Identify the parasite.
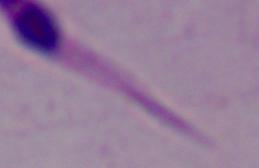
This is Leishmania.

Captured at 1000x magnification. Photomicrograph.